Comment on the morphology of the erythrocytes.
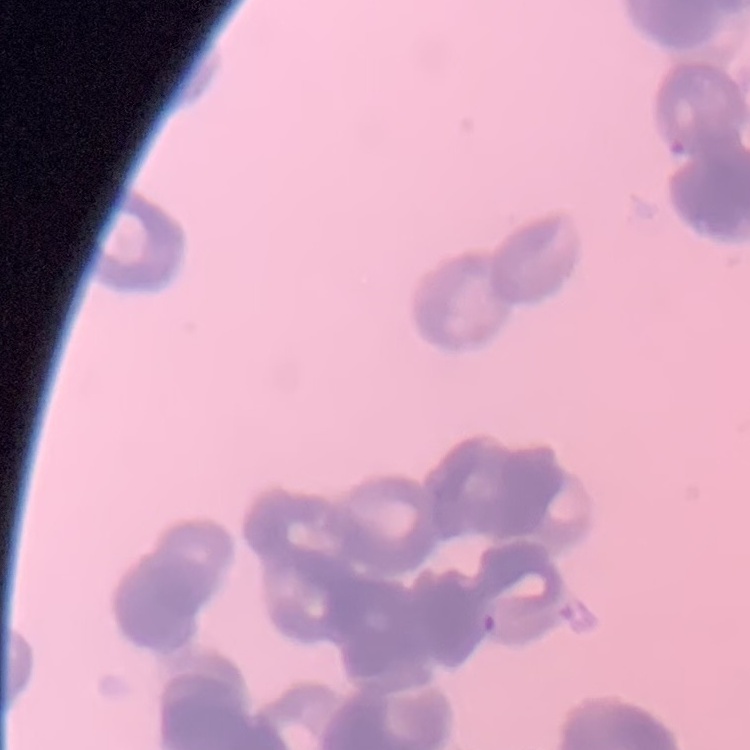
They show rouleaux formation.

Field's or Giemsa stain. Square crop of a larger photomicrograph. Thin blood smear.